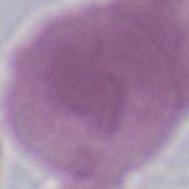

Summary:
  - Identification: red blood cell
  - Magnification: 1000x
  - Modality: micrograph